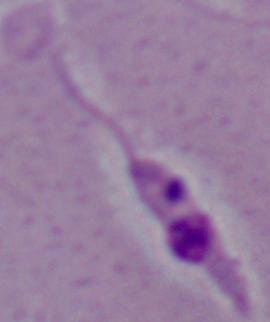
{
  "magnification": "1000x",
  "modality": "photomicrograph",
  "identification": "Leishmania"
}